Locate every Babesia divergens-infected red blood cell.
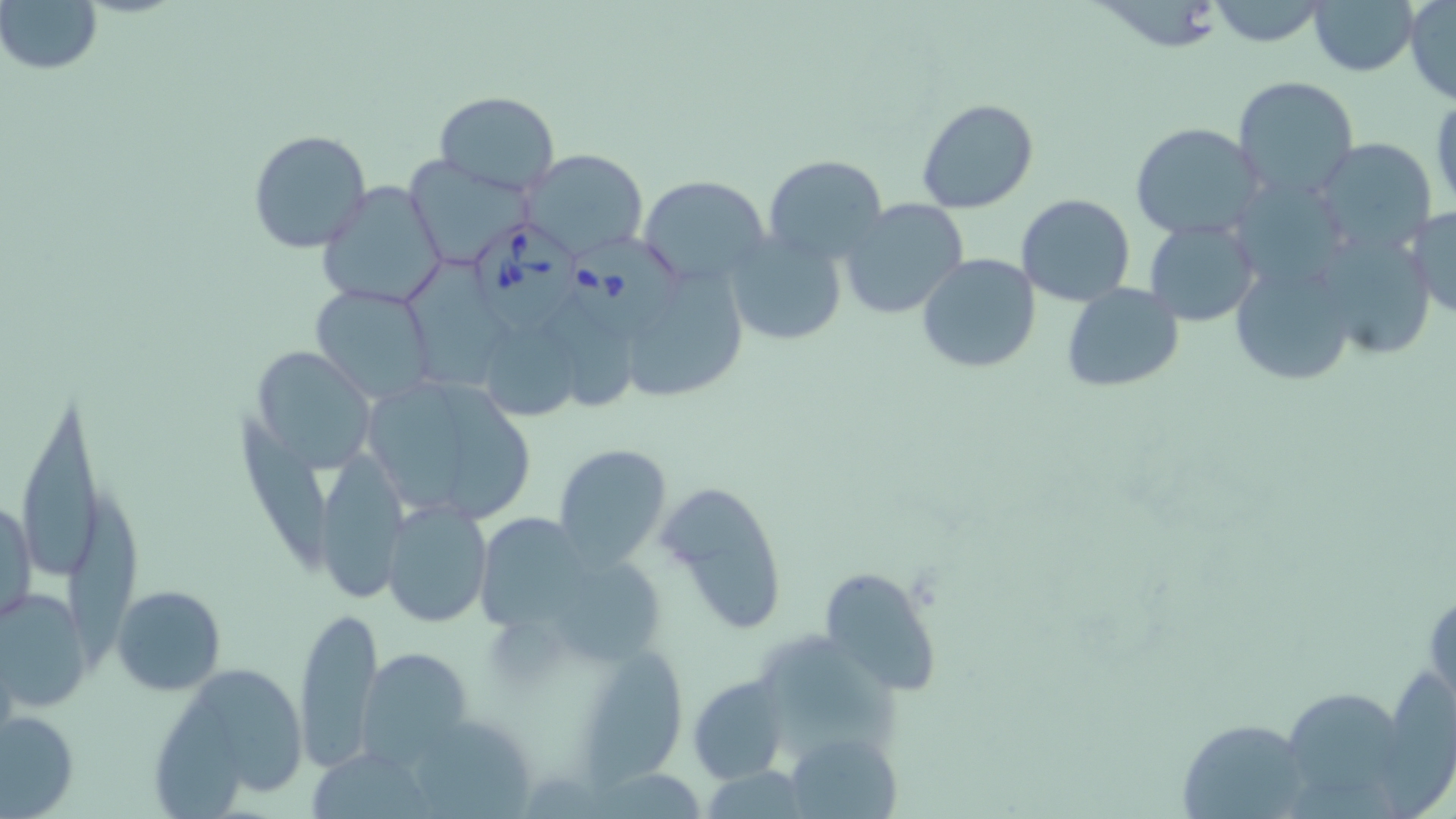

Approximate bounding boxes as (x1,y1)-(x2,y2) corner pairs in pixels.
Babesia divergens-infected red blood cells: (473,217)-(589,334), (572,234)-(690,341).

slide-level diagnosis = Babesia divergens
modality = light microscopy
stain = May-Grünwald-Giemsa
field of view = one of a larger specimen
image size = 1456×819 pixels
magnification = 1000x
uninfected red blood cell locations = approximate bounding boxes as (x1,y1)-(x2,y2) corner pairs in pixels: (0,0)-(102,75), (1206,0)-(1331,46), (1309,0)-(1419,76), (1404,0)-(1456,105), (1232,75)-(1360,200), (433,90)-(560,195), (1429,94)-(1456,215), (916,99)-(1038,214), (1130,121)-(1265,240), (247,129)-(371,252), (1314,140)-(1436,255), (523,148)-(649,262), (407,154)-(534,268), (763,155)-(889,267), (778,170)-(959,295), (638,174)-(772,286), (318,181)-(447,310), (1016,195)-(1137,306), (837,198)-(969,320), (1407,204)-(1456,320), (1144,218)-(1259,328), (1312,227)-(1437,360), (724,232)-(847,346), (916,253)-(1041,374), (402,257)-(508,385), (1232,267)-(1358,386), (633,271)-(749,399), (1062,284)-(1185,393), (310,286)-(436,404), (482,320)-(596,421), (258,345)-(373,473), (436,375)-(537,514), (19,395)-(99,570), (229,413)-(333,568), (551,443)-(672,569), (319,444)-(412,601), (661,481)-(791,631), (1,494)-(37,627), (383,498)-(491,627), (478,508)-(594,634), (552,545)-(665,664), (819,565)-(943,697), (113,584)-(226,696), (0,587)-(90,709), (294,605)-(384,772), (580,647)-(686,791), (356,648)-(473,765), (160,660)-(310,805), (687,676)-(789,783), (1285,685)-(1396,793), (1,709)-(79,816), (1177,718)-(1313,817), (785,732)-(904,819)
preparation = thin blood smear